Assess this cell for malaria.
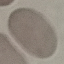
Uninfected.

Summary:
  - Stain: Giemsa
  - Capture: smartphone through the microscope eyepiece
  - Image type: cell patch, automatically extracted from a larger field of view and resized to 64 × 64 pixels
  - Preparation: thin blood smear